Locate every blood parasite and identify its species.
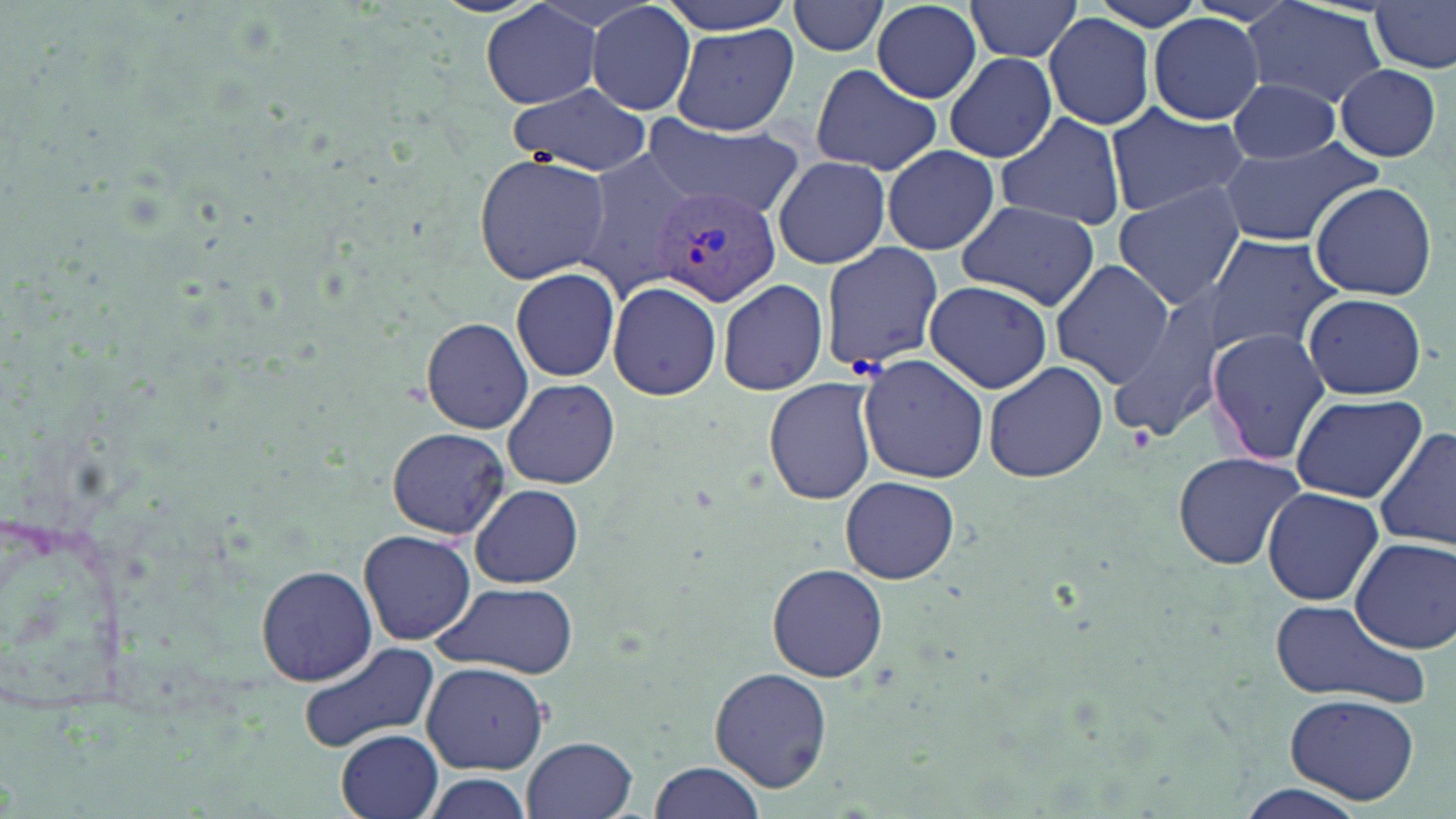

Approximate bounding boxes as [x1, y1, x2, y2] in pixels.
Plasmodium vivax-infected red blood cells: [655, 182, 785, 308].
No Plasmodium falciparum, Plasmodium ovale, Plasmodium malariae, Babesia divergens, or Trypanosoma brucei observed.

Uninfected red blood cell locations: [660, 0, 801, 33], [964, 0, 1085, 62], [1079, 0, 1221, 33], [1244, 0, 1390, 109], [788, 1, 892, 57], [481, 2, 605, 110], [585, 2, 697, 116], [1369, 2, 1455, 73], [871, 3, 984, 101], [1043, 11, 1159, 131], [1149, 13, 1266, 126], [671, 24, 799, 136], [943, 52, 1058, 163], [1334, 61, 1444, 162], [808, 66, 943, 174], [1221, 78, 1344, 163], [510, 83, 653, 176], [1103, 105, 1249, 218], [993, 112, 1128, 230], [641, 114, 807, 222], [1217, 137, 1385, 246], [880, 144, 1002, 257], [575, 151, 699, 293], [473, 153, 611, 283], [773, 155, 890, 269], [1308, 181, 1440, 302], [1112, 182, 1246, 309], [954, 201, 1101, 308], [1205, 235, 1342, 355], [821, 243, 944, 371], [1050, 259, 1174, 390], [510, 266, 621, 383], [717, 278, 830, 397], [606, 280, 723, 402], [923, 281, 1053, 393], [1104, 289, 1241, 446], [1301, 292, 1428, 400], [420, 316, 534, 432], [1205, 328, 1332, 467], [856, 354, 989, 483], [983, 360, 1108, 484], [763, 377, 880, 505], [502, 378, 620, 490], [1291, 393, 1428, 499], [387, 428, 511, 537], [1373, 429, 1456, 550], [1172, 451, 1307, 571], [841, 475, 959, 585], [470, 484, 584, 588], [1263, 486, 1384, 605], [0, 515, 146, 724], [358, 530, 476, 645], [1349, 535, 1456, 654], [768, 562, 887, 681], [256, 564, 376, 685], [431, 580, 578, 677], [1268, 599, 1433, 711], [296, 641, 441, 755], [421, 661, 549, 774], [710, 667, 833, 792], [1283, 692, 1423, 808], [337, 729, 445, 819], [524, 735, 640, 819], [645, 761, 767, 819], [1236, 781, 1363, 819]. Slide-level diagnosis: Plasmodium vivax. May-Grünwald-Giemsa stain. Image is 1456×819 pixels. Optical microscopy. One field of a larger specimen. Captured at 1000x magnification. Thin blood film.